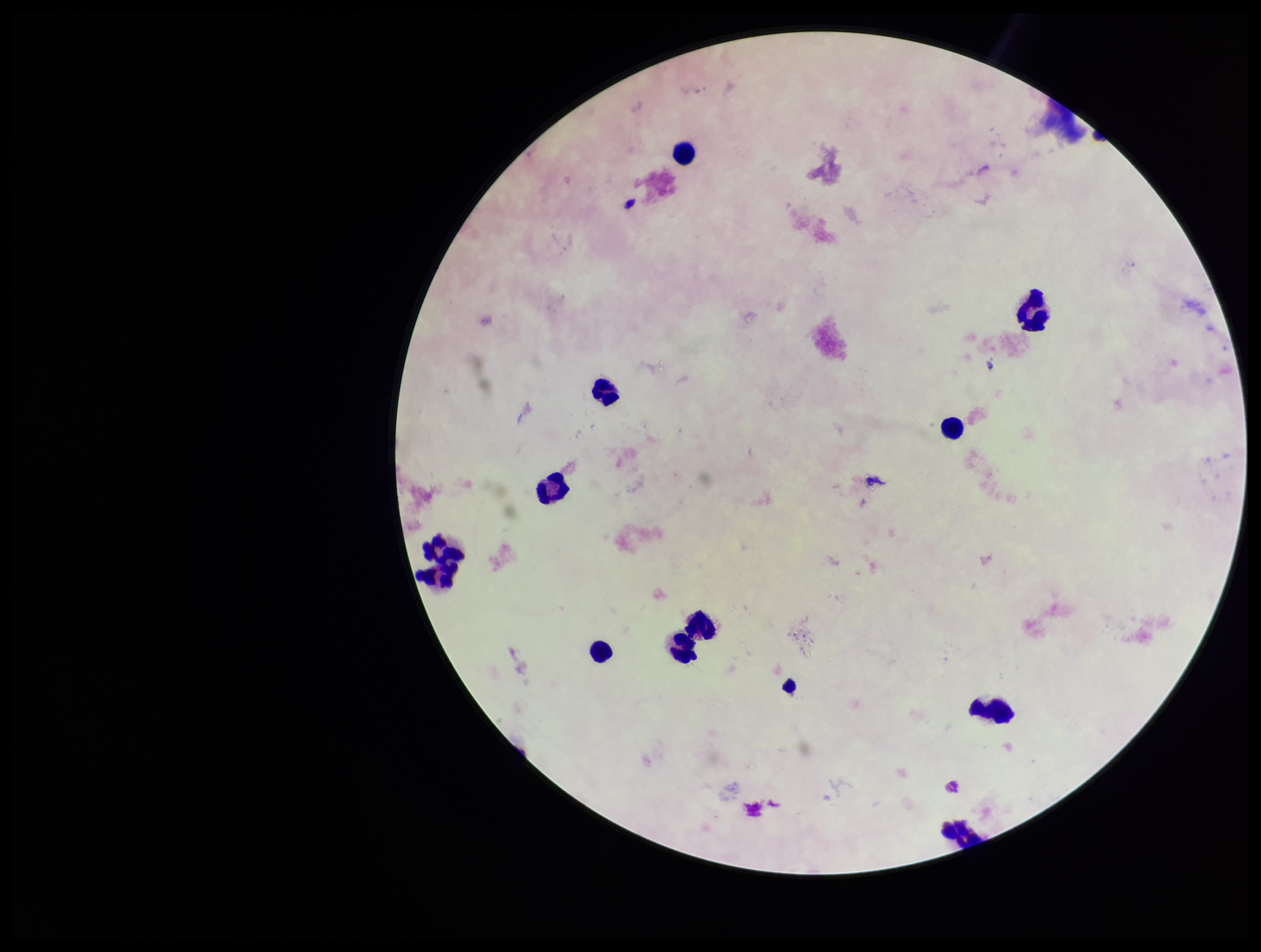
stain = Giemsa
patient malaria status = positive
capture = smartphone photograph through the microscope eyepiece
parasite count = 0
image size = 1261×952 pixels
leukocyte count = 11
preparation = thick blood smear
species reported for this patient = Plasmodium falciparum
Plasmodium parasites = none seen
field of view = one from this slide